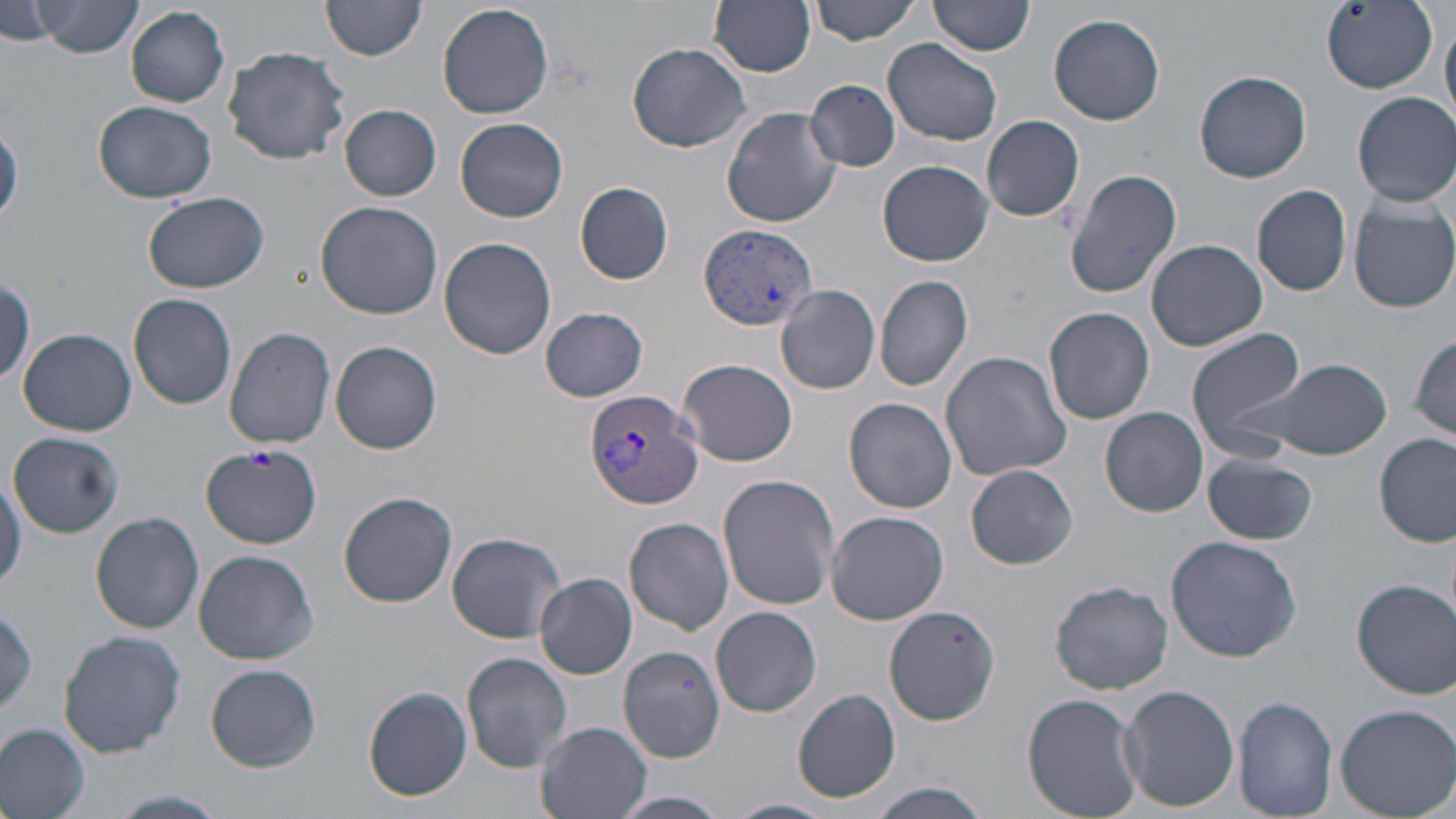 Approximate bounding boxes as named x1/y1/x2/y2 corners in pixels. Plasmodium vivax-infected red blood cell locations: (x1=699, y1=224, x2=817, y2=329), (x1=587, y1=388, x2=704, y2=509). Platelet locations: (x1=246, y1=448, x2=275, y2=471). Uninfected red blood cell locations: (x1=33, y1=0, x2=145, y2=56), (x1=931, y1=0, x2=1035, y2=57), (x1=1, y1=1, x2=62, y2=44), (x1=708, y1=1, x2=815, y2=76), (x1=812, y1=1, x2=923, y2=44), (x1=1322, y1=1, x2=1437, y2=94), (x1=320, y1=2, x2=426, y2=63), (x1=438, y1=2, x2=555, y2=119), (x1=127, y1=6, x2=231, y2=107), (x1=1441, y1=10, x2=1456, y2=130), (x1=1049, y1=13, x2=1166, y2=125), (x1=881, y1=37, x2=1005, y2=146), (x1=627, y1=41, x2=753, y2=152), (x1=222, y1=44, x2=351, y2=165), (x1=1193, y1=69, x2=1312, y2=184), (x1=808, y1=78, x2=898, y2=170), (x1=1352, y1=92, x2=1456, y2=206), (x1=92, y1=100, x2=220, y2=201), (x1=339, y1=104, x2=442, y2=201), (x1=722, y1=106, x2=842, y2=227), (x1=981, y1=113, x2=1083, y2=221), (x1=456, y1=117, x2=569, y2=222), (x1=0, y1=123, x2=23, y2=224), (x1=878, y1=160, x2=993, y2=267), (x1=1063, y1=168, x2=1184, y2=299), (x1=575, y1=182, x2=675, y2=284), (x1=1252, y1=183, x2=1353, y2=296), (x1=144, y1=190, x2=271, y2=292), (x1=1350, y1=199, x2=1456, y2=313), (x1=315, y1=200, x2=443, y2=319), (x1=438, y1=237, x2=558, y2=359), (x1=1145, y1=239, x2=1267, y2=351), (x1=874, y1=274, x2=973, y2=390), (x1=776, y1=284, x2=881, y2=395), (x1=129, y1=292, x2=238, y2=409), (x1=1044, y1=306, x2=1155, y2=425), (x1=539, y1=307, x2=650, y2=402), (x1=224, y1=325, x2=337, y2=448), (x1=1186, y1=327, x2=1311, y2=454), (x1=19, y1=328, x2=136, y2=436), (x1=1409, y1=331, x2=1456, y2=443), (x1=331, y1=340, x2=443, y2=455), (x1=940, y1=351, x2=1072, y2=482), (x1=678, y1=358, x2=798, y2=466), (x1=1263, y1=360, x2=1391, y2=461), (x1=845, y1=397, x2=957, y2=513), (x1=1100, y1=407, x2=1208, y2=516), (x1=9, y1=431, x2=124, y2=535), (x1=1375, y1=432, x2=1455, y2=549), (x1=200, y1=444, x2=322, y2=547), (x1=1203, y1=455, x2=1316, y2=546), (x1=966, y1=464, x2=1079, y2=569), (x1=0, y1=466, x2=25, y2=594), (x1=717, y1=474, x2=841, y2=613), (x1=338, y1=490, x2=458, y2=608), (x1=826, y1=510, x2=947, y2=625), (x1=91, y1=512, x2=205, y2=633), (x1=625, y1=517, x2=735, y2=635), (x1=445, y1=531, x2=567, y2=643), (x1=1164, y1=535, x2=1302, y2=663), (x1=194, y1=549, x2=318, y2=664), (x1=534, y1=573, x2=638, y2=679), (x1=1351, y1=577, x2=1454, y2=698), (x1=1050, y1=580, x2=1173, y2=694), (x1=1, y1=605, x2=39, y2=719), (x1=884, y1=605, x2=1000, y2=724), (x1=710, y1=606, x2=822, y2=717), (x1=57, y1=630, x2=187, y2=756), (x1=618, y1=646, x2=725, y2=764), (x1=462, y1=652, x2=574, y2=773), (x1=206, y1=664, x2=322, y2=771), (x1=364, y1=685, x2=472, y2=801), (x1=1118, y1=686, x2=1238, y2=810), (x1=792, y1=688, x2=902, y2=803), (x1=1023, y1=692, x2=1144, y2=818), (x1=1234, y1=697, x2=1337, y2=819), (x1=1334, y1=702, x2=1456, y2=816), (x1=535, y1=721, x2=653, y2=819), (x1=0, y1=723, x2=90, y2=819), (x1=864, y1=782, x2=993, y2=818), (x1=113, y1=790, x2=229, y2=817), (x1=612, y1=791, x2=729, y2=819), (x1=722, y1=797, x2=835, y2=819). Slide-level diagnosis: Plasmodium vivax. Optical microscopy. May-Grünwald-Giemsa-stained preparation. Thin blood film. One field of a larger specimen. Image is 1456×819 pixels. Captured at 1000x magnification.